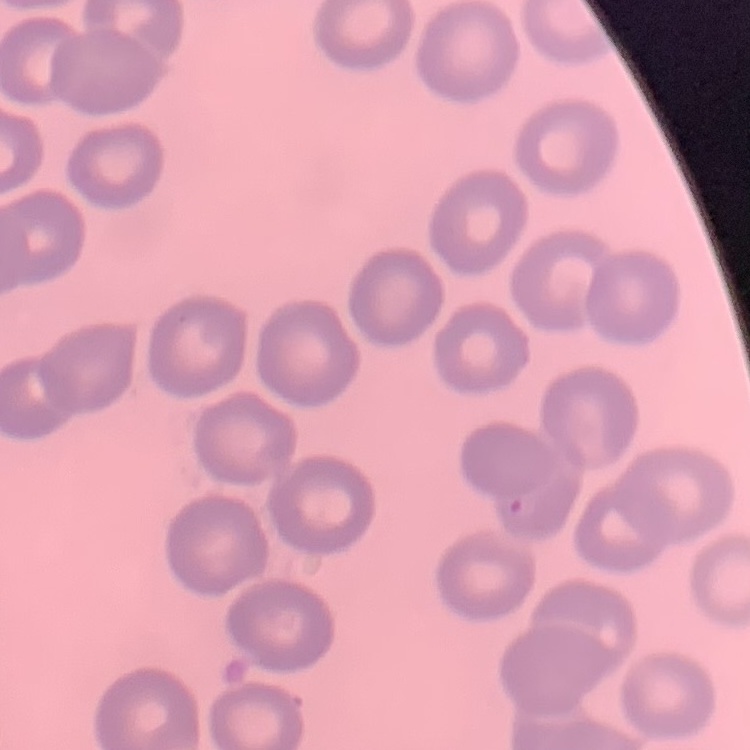 The erythrocytes exhibit no rouleaux formation. One tile cut from a larger photomicrograph. Thin blood film. Stained with either Field's or Giemsa.